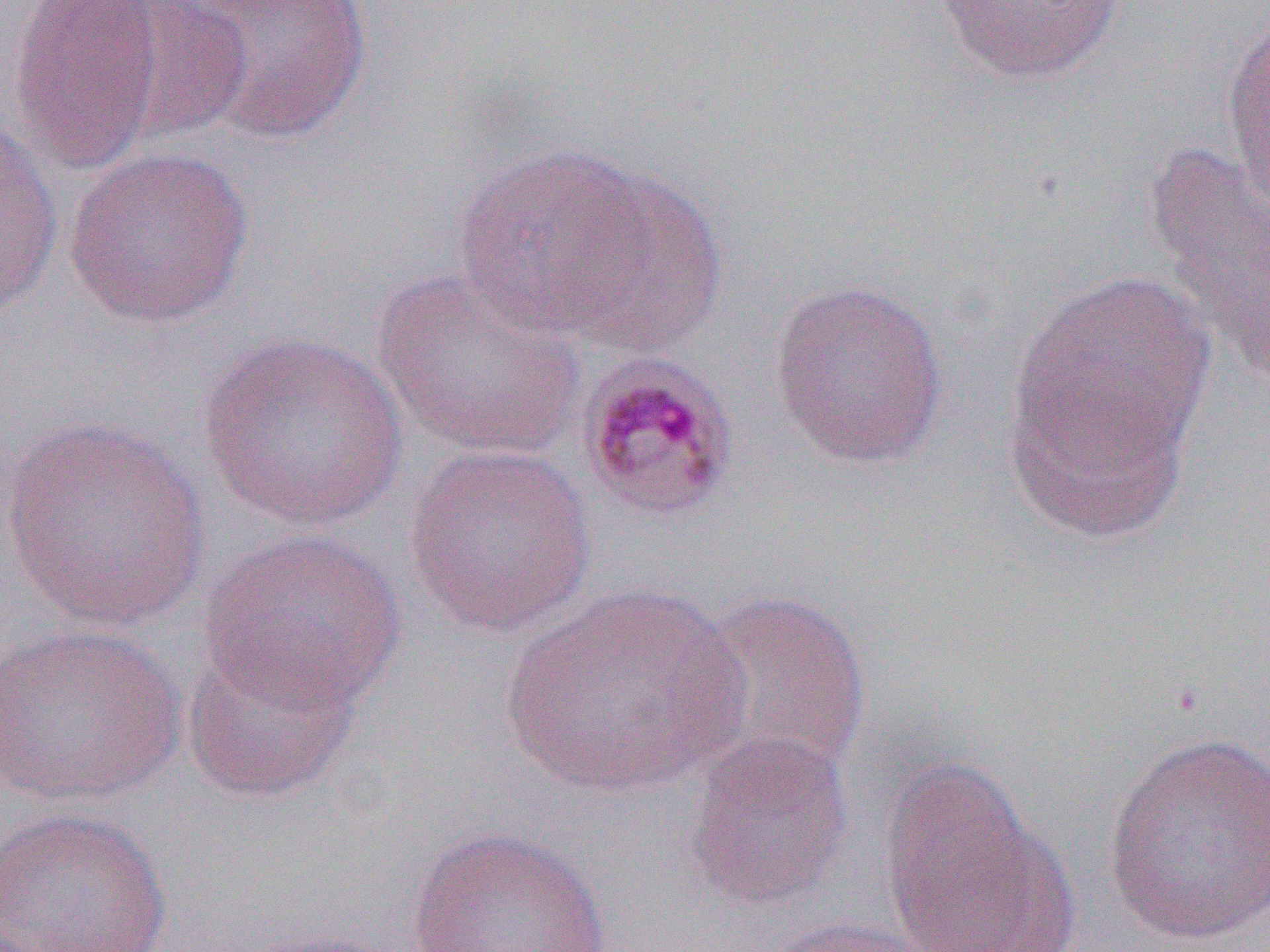

slide-level diagnosis = Plasmodium malariae
image size = 1270×952 pixels
field of view = one of a larger specimen
magnification = 1000x
preparation = thin blood smear
uninfected red blood cell locations = approximate bounding boxes as (x1, y1, x2, y2) in pixels: (104, 0, 251, 143), (168, 0, 374, 145), (935, 0, 1128, 85), (5, 1, 168, 174), (1220, 10, 1269, 216), (0, 117, 64, 321), (1139, 139, 1270, 388), (449, 142, 664, 344), (62, 145, 255, 329), (563, 171, 729, 355), (371, 267, 586, 462), (768, 277, 951, 471), (1005, 278, 1212, 531), (198, 329, 407, 533), (0, 415, 214, 633), (404, 441, 595, 638), (200, 528, 406, 716), (501, 584, 746, 800), (687, 588, 873, 781), (0, 620, 185, 809), (180, 638, 362, 806), (682, 729, 856, 911), (1102, 732, 1270, 950), (876, 758, 1073, 952), (0, 807, 173, 952), (405, 826, 613, 951), (749, 914, 942, 952), (225, 924, 415, 952)
Plasmodium malariae-infected red blood cell locations = approximate bounding boxes as (x1, y1, x2, y2) in pixels: (574, 352, 742, 525)
modality = optical microscopy